State the blood parasite species.
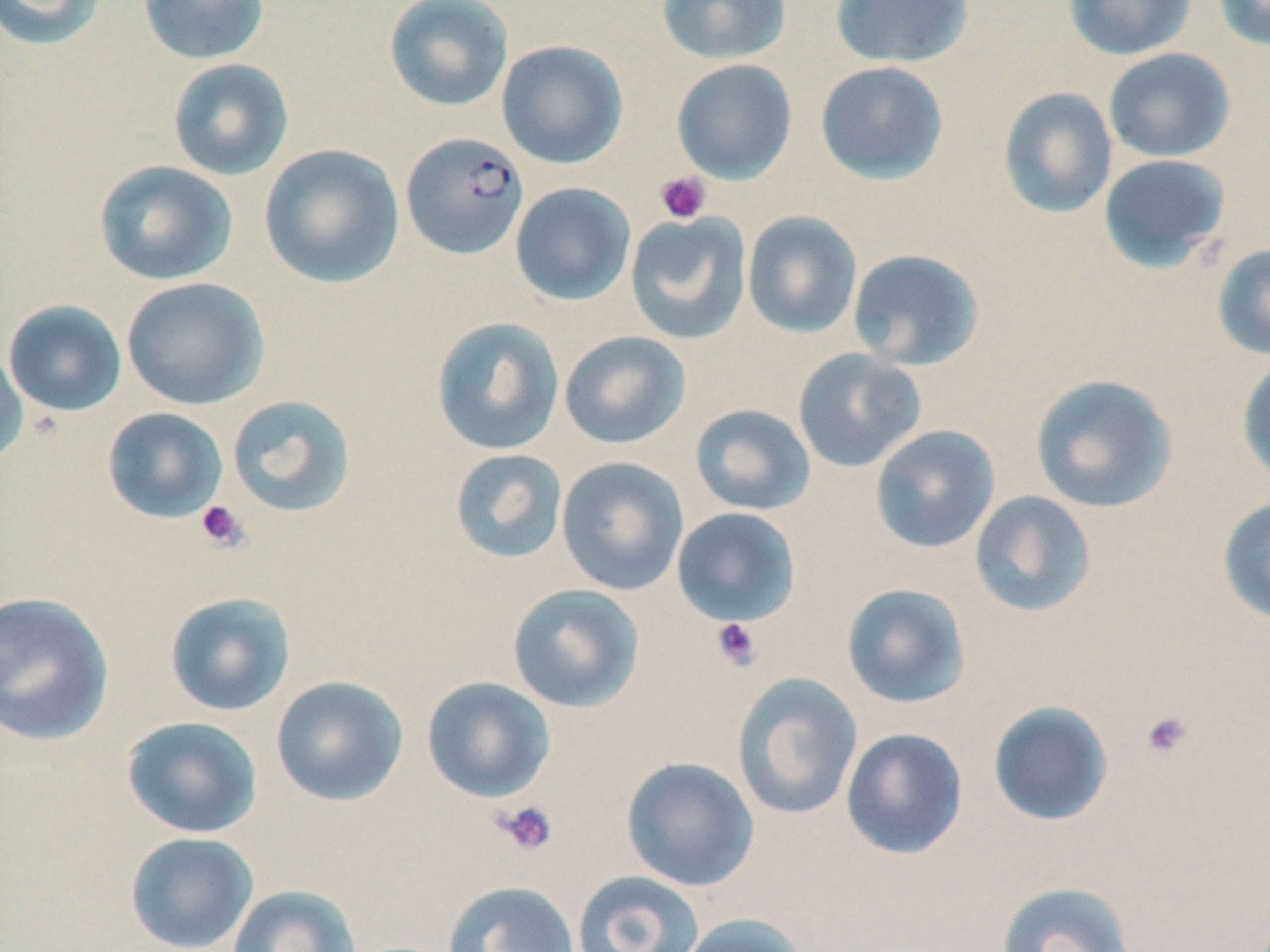
Plasmodium falciparum.

Summary:
  - Coordinate format: approximate bounding boxes as (x1,y1)-(x2,y2) corner pairs in pixels
  - Uninfected red blood cell locations: (0,0)-(109,50), (138,0)-(270,65), (383,0)-(514,112), (656,0)-(791,65), (830,0)-(974,68), (1063,0)-(1196,60), (1212,0)-(1270,52), (496,40)-(629,169), (1103,48)-(1235,162), (167,58)-(294,181), (671,59)-(797,184), (815,61)-(949,184), (998,86)-(1118,219), (258,143)-(404,289), (1098,153)-(1233,273), (93,159)-(238,286), (510,182)-(636,306), (742,211)-(863,339), (624,212)-(753,345), (1211,243)-(1270,361), (847,248)-(985,371), (121,277)-(269,410), (2,300)-(128,417), (430,316)-(565,456), (559,331)-(691,449), (0,345)-(29,467), (792,348)-(926,472), (1236,356)-(1270,488), (1029,374)-(1178,513), (226,394)-(357,517), (689,404)-(816,516), (102,407)-(228,523), (869,424)-(1000,554), (449,448)-(568,564), (556,457)-(689,596), (969,491)-(1097,617), (1217,495)-(1270,626), (671,507)-(802,627), (506,583)-(645,713), (841,583)-(971,709), (0,591)-(115,746), (164,591)-(297,716), (732,673)-(862,820), (270,675)-(409,806), (421,676)-(556,803), (987,700)-(1115,827), (122,716)-(263,838), (840,727)-(968,860), (620,756)-(759,891), (124,831)-(259,951), (571,870)-(705,952), (442,881)-(580,952), (995,881)-(1135,952), (227,884)-(361,952), (676,912)-(809,952)
  - Plasmodium falciparum-infected red blood cell locations: (401,132)-(529,259)
  - Platelet locations: (655,171)-(711,224), (195,500)-(249,552), (710,617)-(762,671), (1140,710)-(1195,760), (494,801)-(558,855)
  - Stain: May-Grünwald-Giemsa
  - Modality: optical microscopy
  - Image size: 1270×952 pixels
  - Field of view: single
  - Magnification: 1000x
  - Preparation: thin blood film